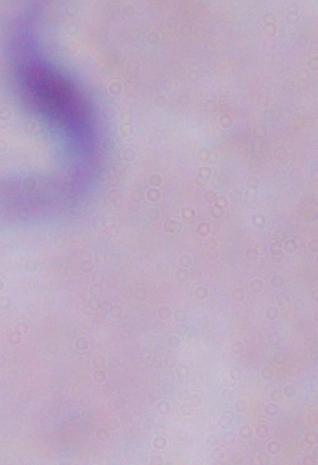
{
  "modality": "micrograph",
  "identification": "trypanosome",
  "magnification": "1000x"
}